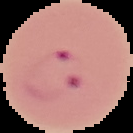

{
  "preparation": "thin blood film",
  "image_type": "segmented cell region on a black background",
  "image_size": "133×133 pixels",
  "result": "malaria parasites detected"
}